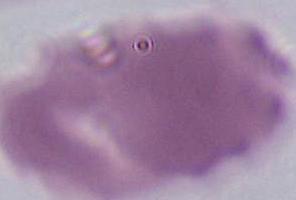

magnification = 1000x
modality = photomicrograph
identification = erythrocyte